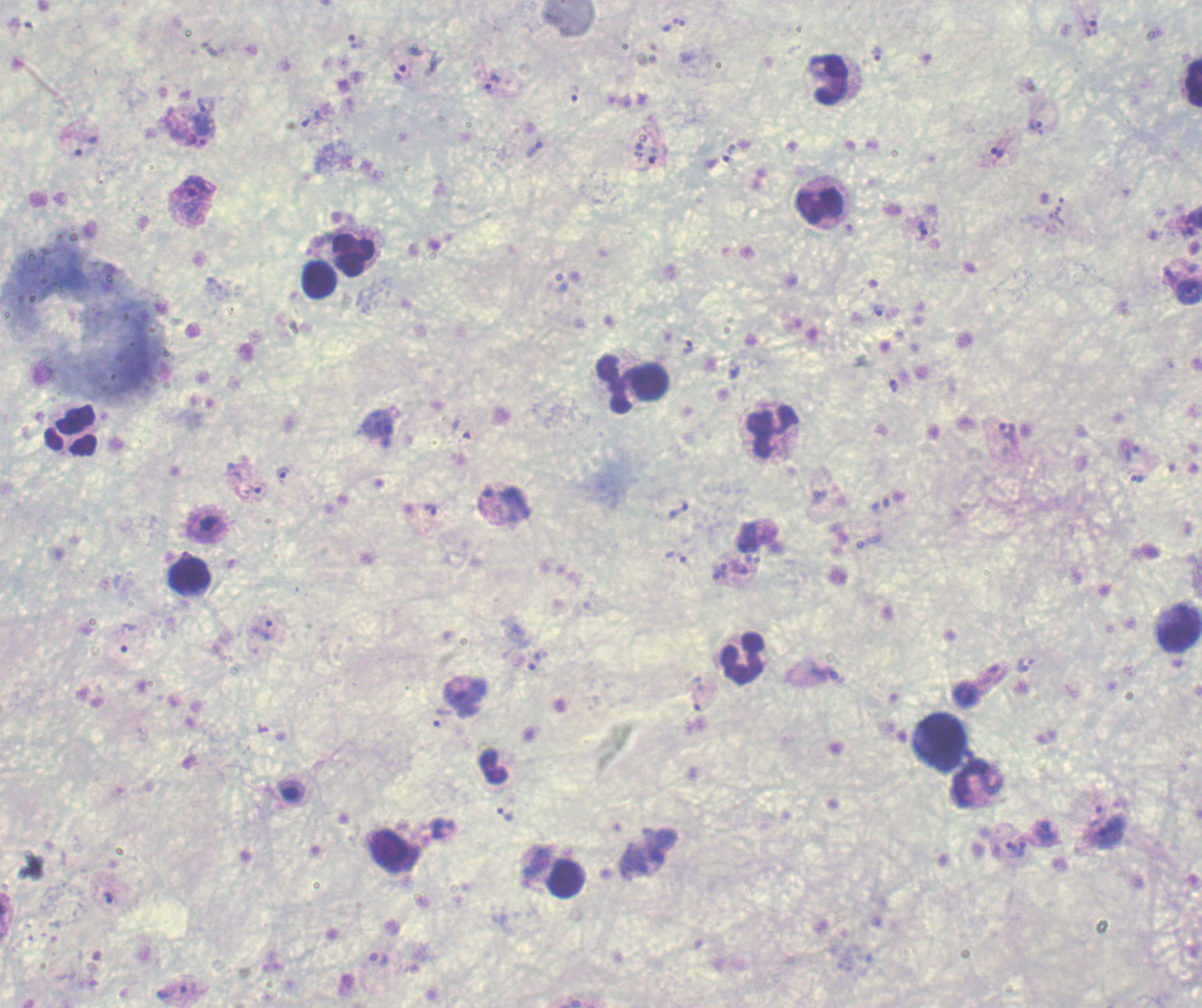
Approximate centers as [x, y] in pixels.
Summary:
  - Leukocyte locations: [831, 79], [1194, 82], [821, 206], [352, 252], [319, 280], [637, 385], [73, 431], [772, 433], [190, 576], [1179, 631], [742, 657], [940, 742], [494, 766], [978, 785], [394, 852], [567, 879]
  - Trophozoite locations: [1091, 28], [877, 55], [400, 72], [491, 81], [575, 93], [206, 105], [310, 118], [202, 124], [1036, 128], [195, 142], [87, 145], [535, 148], [998, 153], [658, 155], [717, 160], [190, 195], [922, 231], [1168, 277], [878, 311], [687, 348], [378, 424], [1006, 430], [1131, 454], [283, 474], [1136, 478], [254, 490], [486, 500], [431, 510], [680, 511], [748, 537], [676, 558], [740, 569], [719, 571], [263, 631], [129, 637], [534, 662], [695, 701], [442, 717], [505, 814], [1096, 816], [1011, 847], [1022, 849], [108, 897], [171, 991]
  - Background quality: poor
  - Result: positive for malaria parasites
  - Preparation: thick smear of blood
  - Context: previously used in a real diagnosis
  - Stain: Romanowsky
  - Field of view: single
  - Image size: 1202×1008 pixels
  - Magnification: 100x